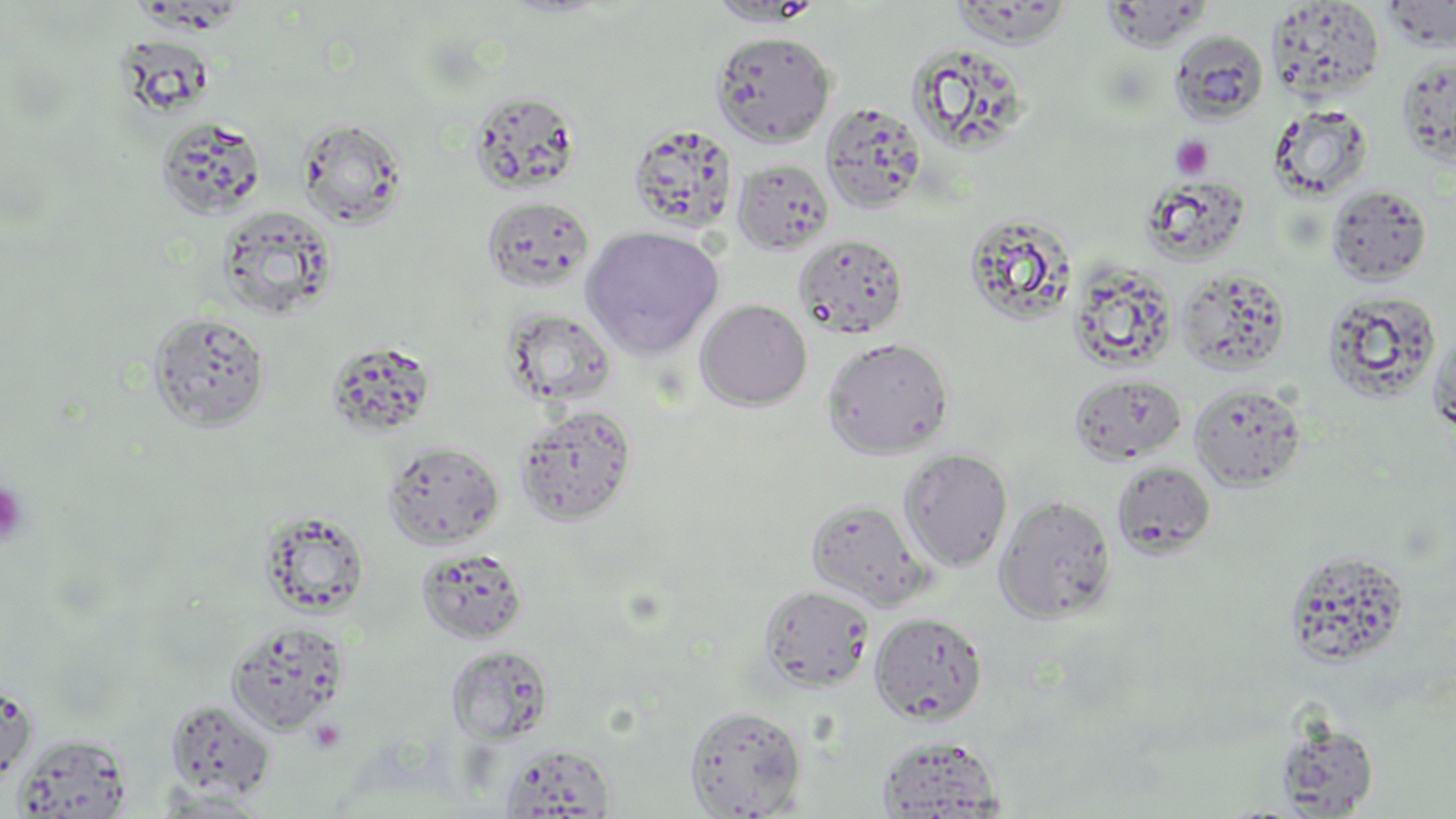

Approximate bounding boxes as (x1,y1)-(x2,y2) corner pairs in pixels. Uninfected red blood cell locations: (707,0)-(824,26), (947,1)-(1075,48), (1100,1)-(1213,52), (1266,1)-(1386,100), (1382,1)-(1456,50), (1169,29)-(1269,125), (711,30)-(836,147), (906,42)-(1032,157), (1396,54)-(1456,169), (468,90)-(582,196), (821,101)-(927,213), (1269,104)-(1374,201), (155,116)-(266,218), (297,117)-(408,229), (628,123)-(739,234), (732,158)-(835,255), (1142,174)-(1251,267), (1326,184)-(1432,285), (482,196)-(595,292), (218,204)-(339,320), (963,211)-(1076,326), (581,225)-(724,359), (794,234)-(909,339), (1067,262)-(1178,373), (1177,268)-(1292,374), (1321,289)-(1442,403), (695,299)-(812,411), (504,309)-(617,406), (148,311)-(272,432), (1428,327)-(1456,440), (822,336)-(955,459), (323,340)-(439,439), (1069,373)-(1187,465), (1189,382)-(1307,491), (515,405)-(636,525), (382,440)-(505,550), (898,448)-(1014,572), (1112,461)-(1217,557), (995,495)-(1118,624), (806,498)-(932,610), (260,511)-(371,617), (415,547)-(529,644), (1283,548)-(1411,668), (758,585)-(875,692), (869,612)-(988,725), (225,620)-(350,734), (446,644)-(553,743), (0,680)-(38,783), (165,699)-(276,801), (683,704)-(808,818), (1274,718)-(1380,817), (13,733)-(133,818), (877,735)-(1005,817), (498,742)-(617,818), (153,789)-(272,817). Platelet locations: (1170,136)-(1213,180), (0,482)-(28,548). Slide-level diagnosis: no evidence of blood parasites. Thin blood smear. 1000x magnification. Single field of view. Image is 1456×819 pixels. May-Grünwald-Giemsa stain. Optical microscopy.